Locate every blood parasite and identify its species.
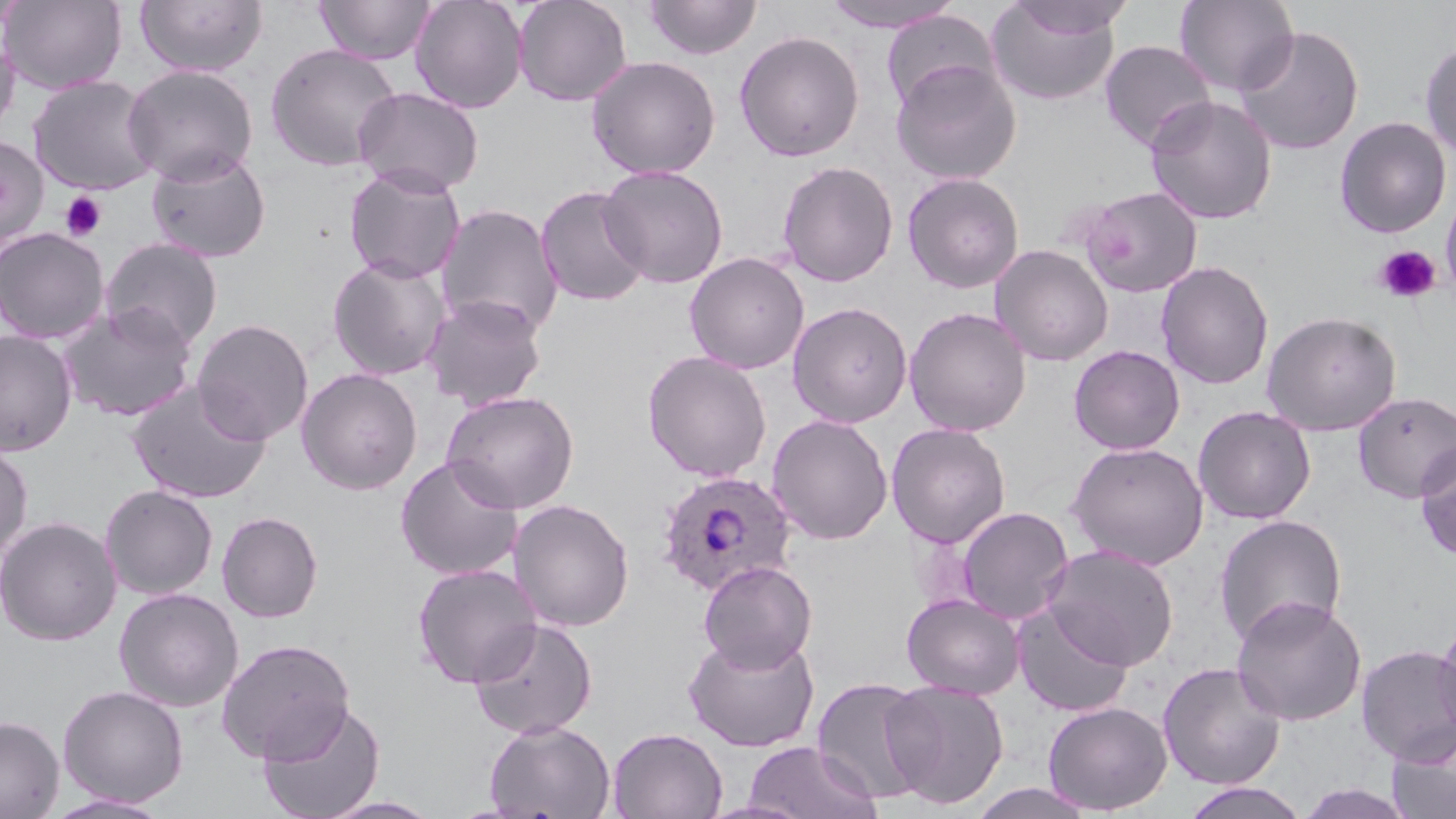
Approximate bounding boxes as (x1,y1)-(x2,y2) corner pairs in pixels.
Plasmodium ovale-infected red blood cells: (655,469)-(799,597).
No Plasmodium falciparum, Plasmodium malariae, Plasmodium vivax, Babesia divergens, or Trypanosoma brucei observed.

slide-level diagnosis = Plasmodium ovale
uninfected red blood cell locations = approximate bounding boxes as (x1,y1)-(x2,y2) corner pairs in pixels: (1,0)-(127,94), (135,0)-(268,77), (315,0)-(436,65), (410,0)-(528,113), (512,0)-(632,107), (643,0)-(761,60), (819,0)-(965,33), (1007,0)-(1136,40), (1174,0)-(1299,97), (985,2)-(1122,107), (880,10)-(999,114), (1233,26)-(1364,155), (734,30)-(865,162), (0,33)-(21,141), (1098,40)-(1217,151), (1420,40)-(1456,162), (265,42)-(402,172), (586,55)-(721,179), (891,59)-(1022,185), (122,64)-(259,184), (27,75)-(161,195), (352,86)-(485,196), (1144,95)-(1277,225), (1334,116)-(1452,238), (0,136)-(49,249), (145,148)-(271,263), (776,160)-(899,287), (343,165)-(466,284), (597,165)-(729,289), (902,172)-(1025,293), (535,185)-(651,307), (1079,185)-(1203,296), (1441,189)-(1456,300), (436,203)-(565,339), (0,226)-(110,344), (100,237)-(223,352), (990,244)-(1113,366), (684,252)-(810,374), (327,256)-(450,380), (1156,261)-(1274,390), (424,293)-(547,411), (787,301)-(913,427), (58,304)-(197,422), (904,306)-(1031,436), (1261,310)-(1402,435), (191,318)-(314,445), (0,329)-(78,456), (1068,344)-(1185,455), (642,350)-(772,482), (296,367)-(423,495), (126,379)-(272,506), (441,390)-(580,514), (1353,391)-(1456,504), (1193,406)-(1316,524), (767,414)-(893,545), (886,422)-(1011,548), (0,438)-(33,562), (1415,440)-(1456,561), (1065,441)-(1209,569), (395,455)-(524,581), (100,484)-(218,600), (508,498)-(635,632), (955,506)-(1074,624), (217,511)-(324,623), (1213,514)-(1348,648), (0,515)-(122,646), (1042,544)-(1179,670), (698,560)-(818,673), (412,562)-(543,689), (112,587)-(244,712), (901,593)-(1025,699), (1230,595)-(1366,726), (1011,601)-(1135,718), (1433,614)-(1456,744), (469,617)-(598,739), (683,631)-(820,751), (216,638)-(355,763), (1356,644)-(1456,764), (1157,661)-(1286,790), (811,676)-(933,804), (881,679)-(1010,809), (57,684)-(189,807), (257,699)-(387,819), (1043,701)-(1173,815), (0,716)-(64,818), (484,719)-(616,819), (607,727)-(727,819), (1386,727)-(1455,819), (744,741)-(883,818), (1296,782)-(1419,818), (968,783)-(1098,818), (1180,783)-(1311,819), (44,794)-(172,818), (319,795)-(445,818)
platelet locations = approximate bounding boxes as (x1,y1)-(x2,y2) corner pairs in pixels: (60,191)-(107,242), (1374,245)-(1441,304)
modality = light microscopy
stain = May-Grünwald-Giemsa
image size = 1456×819 pixels
preparation = thin blood smear
magnification = 1000x
field of view = one of a larger specimen